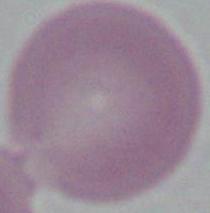

modality = photomicrograph
identification = red blood cell
magnification = 1000x